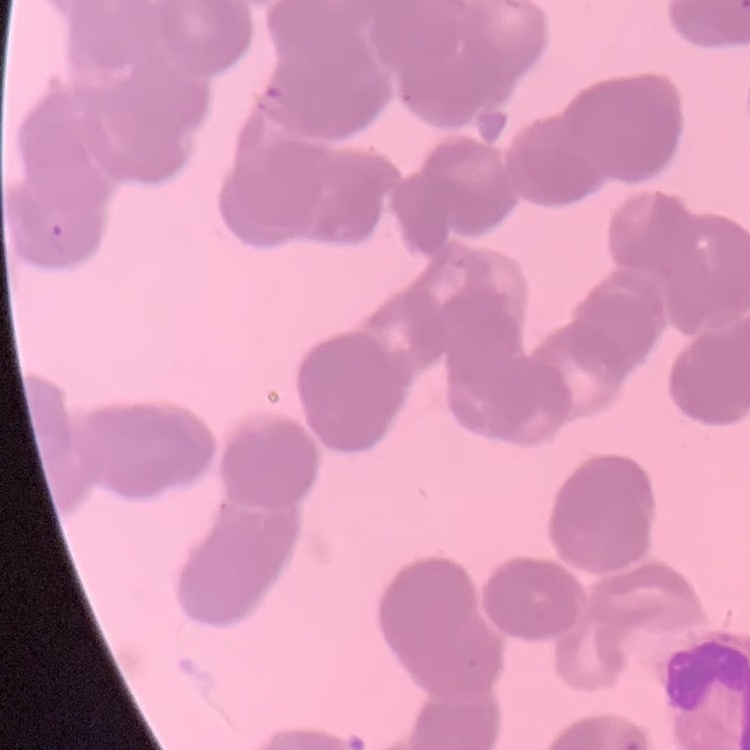
The red blood cells exhibit rouleaux formation. Thin peripheral smear. Field's or Giemsa stain. One tile cut from a larger photomicrograph.